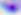

Summary:
  - Identification: Toxoplasma gondii
  - Modality: micrograph
  - Magnification: 400x